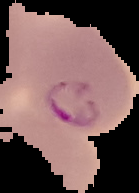

Image is 139×193 pixels. From a thin blood smear. Segmented cell region on a black background. Malaria status: parasitized.